Identify the parasite.
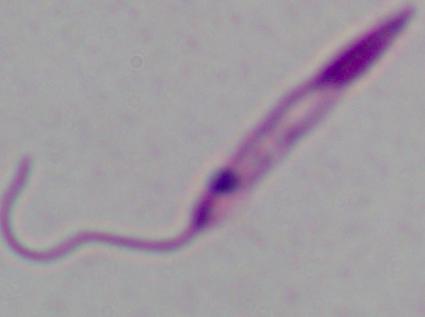
Leishmania.

Summary:
  - Magnification: 1000x
  - Modality: micrograph